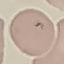

Result: no malaria parasites detected. Giemsa-stained preparation. Thin smear of blood. Automatically extracted cell patch, resized to 64 × 64 pixels. Acquired by smartphone through the microscope eyepiece.